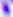

{
  "identification": "Toxoplasma gondii",
  "magnification": "400x",
  "modality": "micrograph"
}